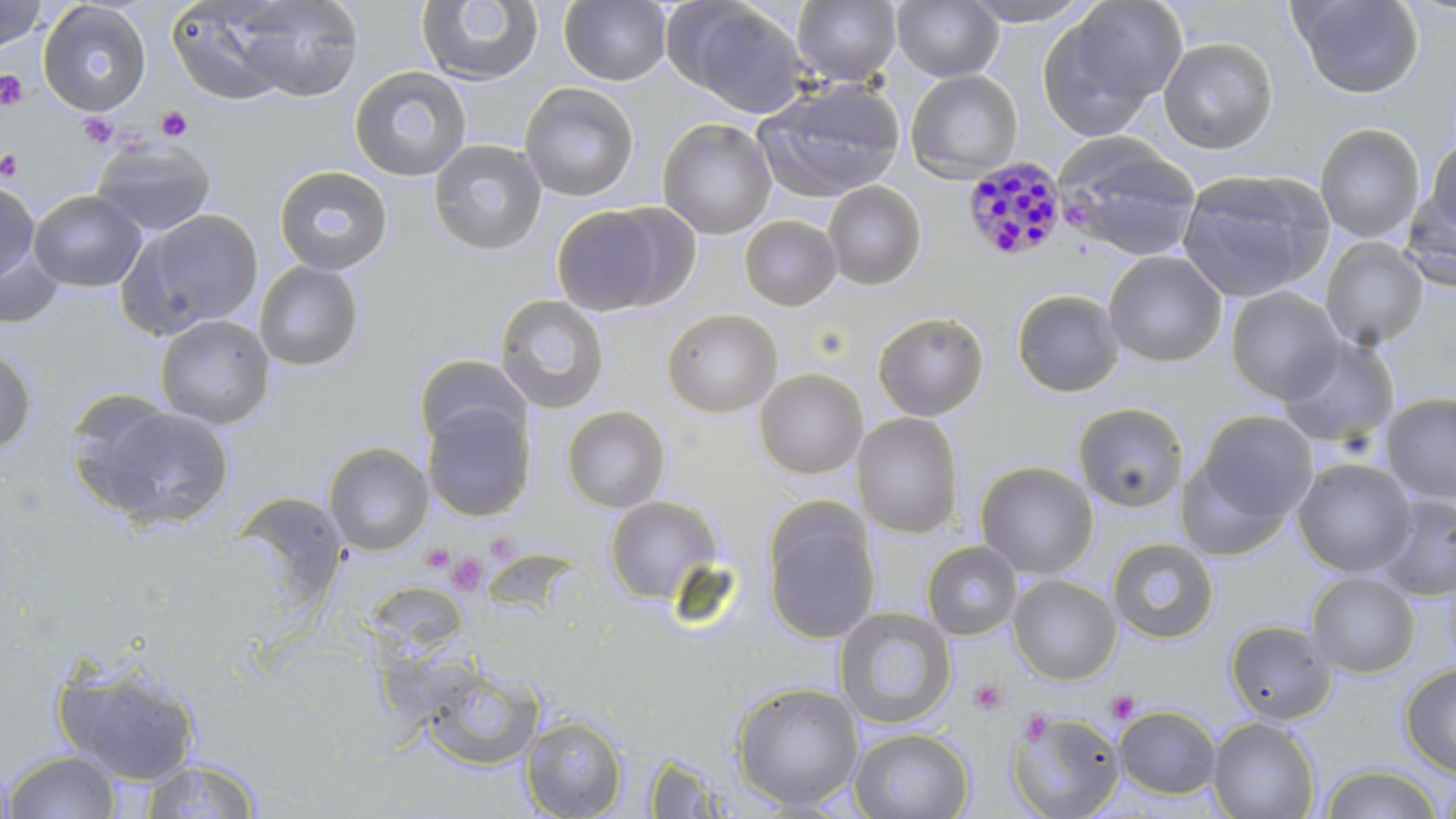 Approximate bounding boxes as [x1, y1, x2, y2] in pixels. Uninfected red blood cell locations: [559, 0, 672, 86], [792, 0, 902, 86], [891, 0, 1004, 82], [958, 0, 1097, 26], [1291, 0, 1424, 99], [0, 1, 48, 54], [416, 1, 544, 86], [38, 2, 151, 116], [204, 2, 366, 103], [669, 2, 812, 118], [1038, 2, 1185, 138], [1158, 36, 1278, 154], [349, 66, 473, 181], [905, 69, 1023, 182], [754, 78, 906, 203], [519, 82, 639, 201], [657, 117, 777, 240], [1314, 123, 1425, 243], [1055, 137, 1203, 262], [1424, 138, 1456, 239], [427, 139, 547, 255], [92, 141, 215, 237], [273, 165, 393, 276], [1176, 168, 1334, 303], [0, 180, 40, 285], [822, 180, 927, 291], [1400, 189, 1456, 293], [28, 190, 147, 292], [551, 204, 682, 317], [121, 209, 265, 337], [739, 215, 842, 311], [1320, 236, 1429, 351], [0, 245, 63, 328], [1103, 251, 1227, 368], [253, 260, 364, 371], [1225, 286, 1345, 404], [1010, 289, 1125, 398], [494, 294, 610, 414], [661, 308, 783, 418], [871, 310, 990, 421], [155, 314, 275, 429], [1277, 337, 1399, 449], [0, 348, 37, 457], [413, 354, 532, 451], [753, 368, 868, 479], [1379, 392, 1456, 506], [76, 401, 236, 531], [422, 401, 535, 522], [1072, 402, 1190, 514], [561, 405, 671, 513], [1195, 410, 1317, 524], [852, 412, 964, 539], [323, 442, 434, 556], [1292, 458, 1417, 577], [1175, 459, 1291, 561], [975, 461, 1098, 580], [227, 492, 349, 615], [1373, 493, 1456, 601], [604, 495, 724, 604], [762, 505, 880, 645], [1107, 536, 1219, 643], [921, 540, 1023, 640], [1305, 570, 1420, 678], [1007, 574, 1122, 685], [364, 582, 471, 662], [834, 606, 956, 730], [1224, 618, 1337, 725], [52, 660, 202, 785], [415, 661, 546, 772], [1399, 663, 1456, 777], [731, 681, 865, 812], [1114, 705, 1221, 799], [1007, 708, 1126, 819], [520, 714, 629, 818], [1207, 716, 1320, 819], [849, 727, 973, 819], [3, 750, 122, 819], [643, 753, 733, 817], [0, 756, 17, 818], [139, 759, 262, 818], [1320, 764, 1443, 819], [1438, 768, 1456, 819]. Plasmodium malariae-infected red blood cell locations: [961, 155, 1068, 263]. Platelet locations: [0, 69, 28, 111], [155, 106, 193, 142], [78, 112, 118, 149], [0, 148, 23, 182], [488, 538, 521, 569], [422, 546, 455, 572], [447, 553, 490, 595], [970, 678, 1008, 715], [1106, 691, 1141, 724], [1020, 710, 1054, 743]. Slide-level diagnosis: Plasmodium malariae. Image is 1456×819 pixels. Thin blood film. Light microscopy. Captured at 1000x magnification. May-Grünwald-Giemsa stain. Single field of view.